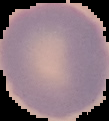

Summary:
  - Image size: 109×121 pixels
  - Preparation: thin blood film
  - Image type: segmented cell region with the area outside set to black
  - Result: negative for Plasmodium parasites